Comment on the morphology of the erythrocytes.
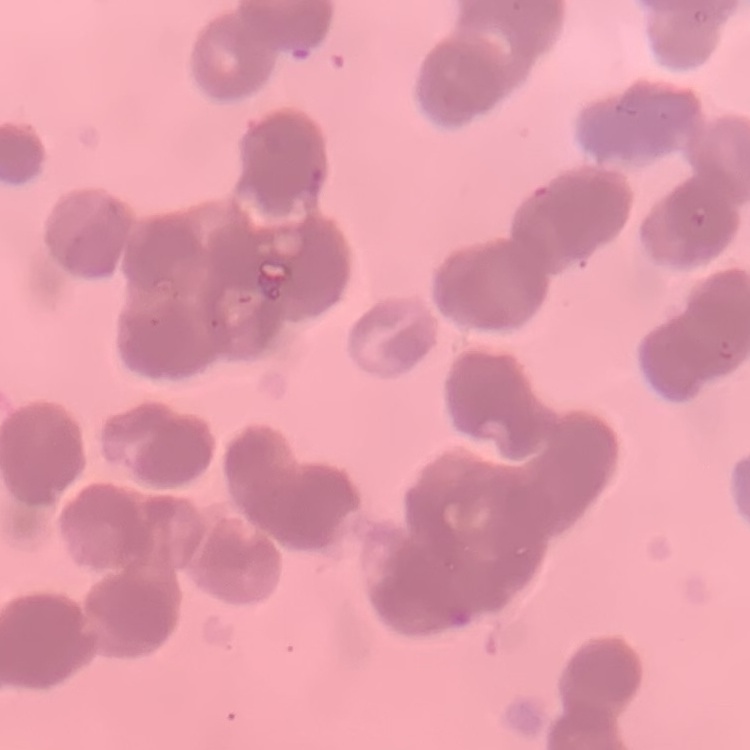
They show rouleaux formation.

Summary:
  - Image type: square crop of a larger photomicrograph
  - Stain: Field's or Giemsa
  - Preparation: thin blood smear